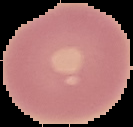
Summary:
  - Preparation: thin blood smear
  - Image size: 133×127 pixels
  - Image type: segmented cell region with the area outside set to black
  - Malaria status: uninfected